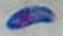
Toxoplasma gondii is shown. Photomicrograph. Captured at 1000x magnification.